Name the cell type shown.
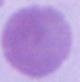
This is an erythrocyte.

Summary:
  - Modality: photomicrograph
  - Magnification: 1000x